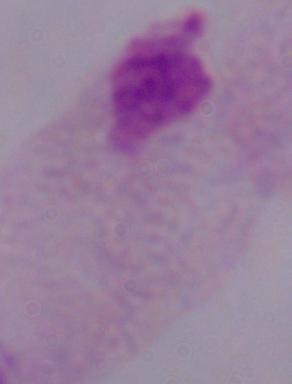

Captured at 1000x magnification. Photomicrograph. A trichomonad is shown.